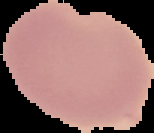 Segmented cell region on a black background. From a thin blood film. Image is 154×133 pixels. Result: no Plasmodium parasites seen.